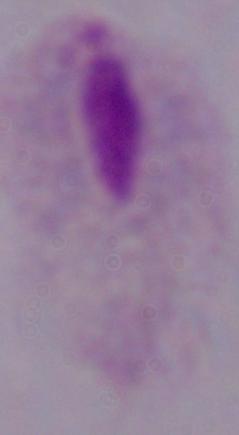 Photomicrograph. 1000x magnification. A trichomonad is shown.